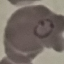
Summary:
  - Result: malaria parasites identified
  - Preparation: thin blood smear
  - Image type: cell patch, automatically extracted from a larger field of view and resized to 64 × 64 pixels
  - Capture: smartphone through the microscope eyepiece
  - Stain: Giemsa